Identify the blood parasite species.
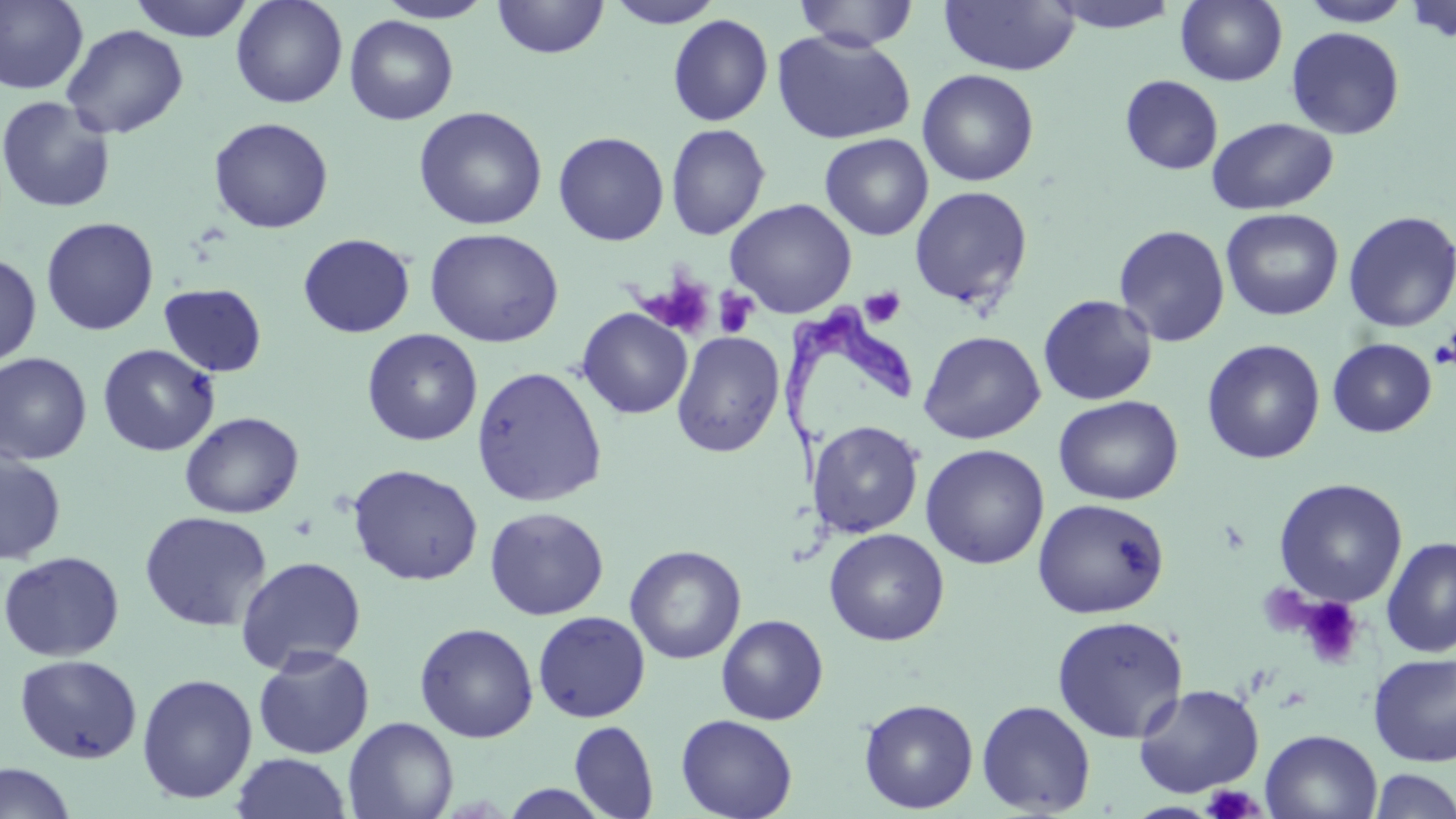
Trypanosoma brucei.

field of view = single
preparation = thin blood smear
uninfected red blood cell locations = approximate bounding boxes as (x1, y1, x2, y2) in pixels: (127, 0, 257, 42), (231, 0, 348, 108), (376, 0, 496, 24), (491, 0, 609, 59), (603, 0, 726, 28), (794, 0, 918, 51), (939, 0, 1081, 77), (1042, 0, 1184, 34), (1175, 0, 1289, 86), (1404, 0, 1456, 45), (0, 1, 89, 94), (1298, 1, 1413, 27), (667, 14, 773, 126), (344, 15, 459, 125), (61, 24, 189, 139), (1286, 26, 1405, 140), (771, 29, 917, 145), (917, 69, 1039, 187), (1119, 74, 1223, 176), (0, 95, 117, 214), (413, 106, 548, 230), (208, 117, 334, 234), (1206, 117, 1339, 216), (665, 123, 770, 241), (553, 131, 670, 246), (820, 133, 934, 241), (908, 185, 1034, 309), (725, 198, 857, 318), (1220, 208, 1343, 321), (1342, 210, 1456, 334), (41, 217, 159, 336), (1113, 224, 1230, 347), (424, 227, 564, 348), (298, 233, 415, 338), (0, 252, 42, 368), (159, 283, 267, 377), (1037, 294, 1157, 406), (576, 308, 693, 419), (362, 328, 483, 446), (918, 330, 1045, 444), (671, 331, 785, 458), (1327, 337, 1437, 437), (1201, 339, 1325, 464), (97, 343, 220, 457), (0, 352, 93, 466), (471, 365, 608, 507), (1054, 395, 1184, 505), (180, 411, 304, 518), (808, 420, 925, 538), (920, 444, 1050, 569), (0, 449, 67, 564), (347, 464, 483, 586), (1273, 477, 1408, 607), (1032, 498, 1170, 619), (484, 506, 609, 620), (139, 510, 272, 632), (823, 528, 949, 646), (1381, 537, 1456, 657), (625, 545, 746, 664), (1, 551, 125, 661), (235, 555, 367, 674), (532, 610, 651, 723), (716, 614, 828, 725), (1051, 614, 1188, 743), (415, 622, 538, 743), (253, 646, 375, 759), (1368, 652, 1456, 766), (15, 654, 143, 765), (136, 673, 258, 804), (1133, 684, 1265, 798), (859, 698, 978, 813), (976, 700, 1097, 817), (675, 714, 797, 819), (343, 717, 459, 819), (569, 720, 659, 818), (1261, 729, 1382, 818), (231, 752, 352, 819), (0, 762, 76, 819), (1366, 769, 1456, 818), (496, 783, 614, 818)
magnification = 1000x
stain = May-Grünwald-Giemsa
Trypanosoma brucei locations = approximate bounding boxes as (x1, y1, x2, y2) in pixels: (782, 304, 922, 492)
image size = 1456×819 pixels
modality = light microscopy
platelet locations = approximate bounding boxes as (x1, y1, x2, y2) in pixels: (639, 270, 716, 339), (860, 287, 905, 328), (714, 288, 759, 338), (1431, 339, 1456, 369), (1297, 595, 1366, 669), (1200, 785, 1266, 818)